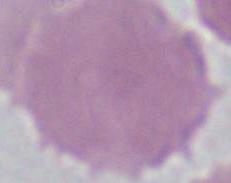 Photomicrograph. Captured at 1000x magnification. A red blood cell is shown.